Name the parasite shown.
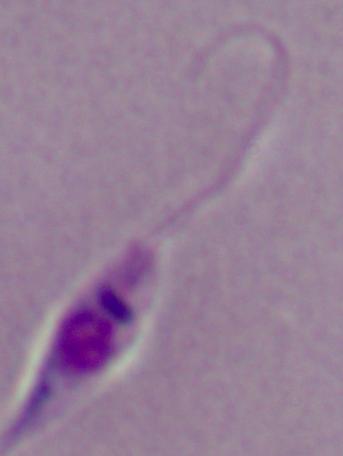

This is Leishmania.

Summary:
  - Modality: photomicrograph
  - Magnification: 1000x